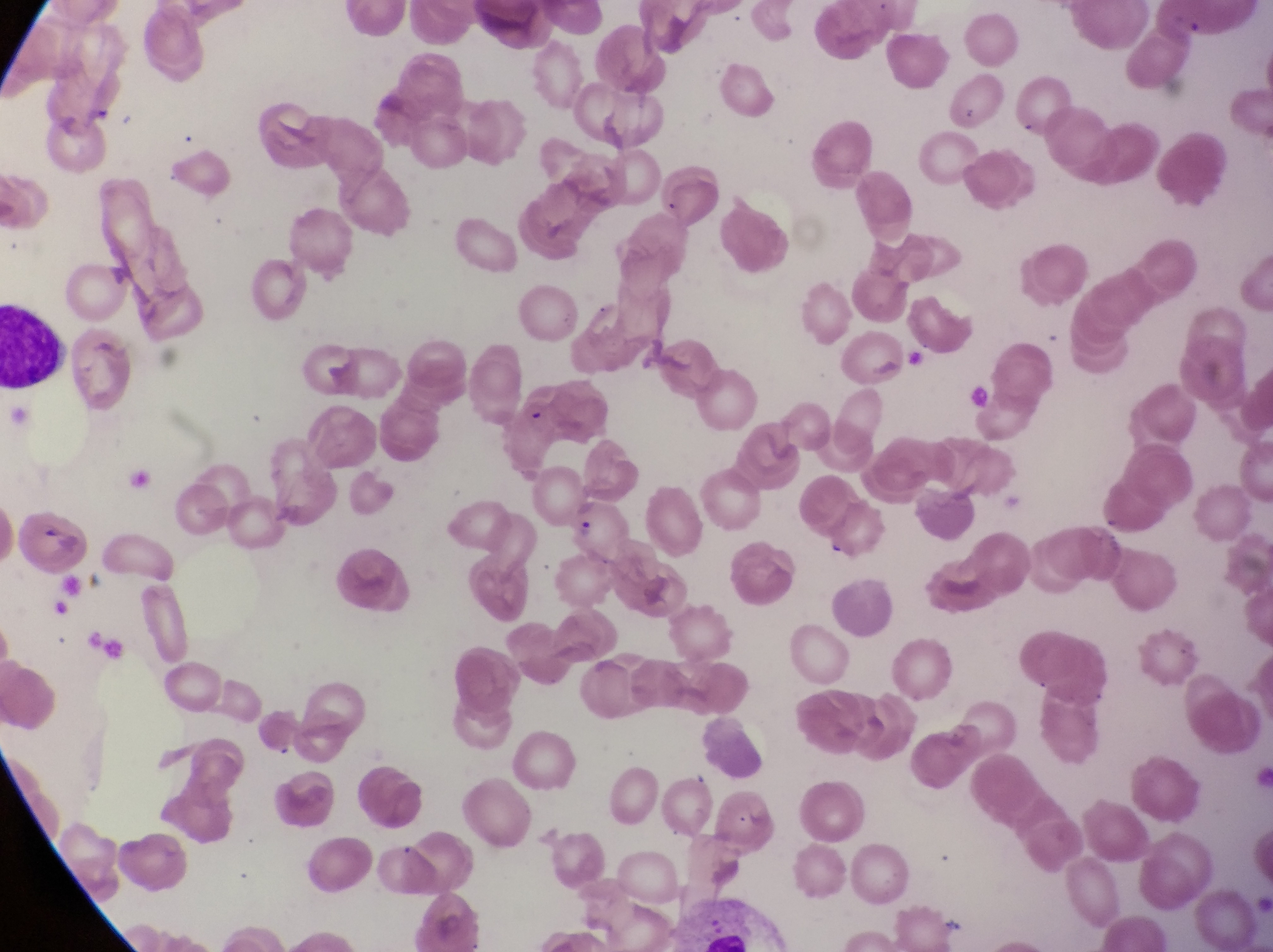

{
  "field_of_view": "single",
  "country": "Uganda",
  "image_size": "1273×952 pixels",
  "magnification": "1000x",
  "parasitised_red_blood_cell_locations": "approximate bounding boxes as (left, top, right, bottom) in pixels: (519, 382, 611, 447), (569, 500, 636, 570)",
  "artifact_platelet_like_body_stain_precipitate_or_debris_locations": "approximate bounding boxes as (left, top, right, bottom) in pixels: (961, 102, 979, 122)",
  "preparation": "thin blood film",
  "capture": "smartphone photograph through the eyepiece of an Olympus CX-23 microscope",
  "leukocyte_locations": "approximate bounding boxes as (left, top, right, bottom) in pixels: (2, 299, 69, 387)"
}